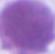 Micrograph. An erythrocyte is seen. Captured at 1000x magnification.